Report the malaria status of this cell.
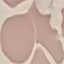

Uninfected.

preparation: thin blood smear
capture: smartphone camera at the microscope eyepiece
stain: Giemsa
image_type: automatically extracted cell patch, resized to 64 × 64 pixels